State which cell type is depicted.
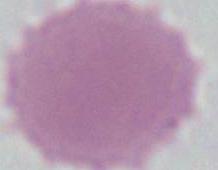
This is an erythrocyte.

magnification = 1000x
modality = micrograph